Describe the morphology of the erythrocytes.
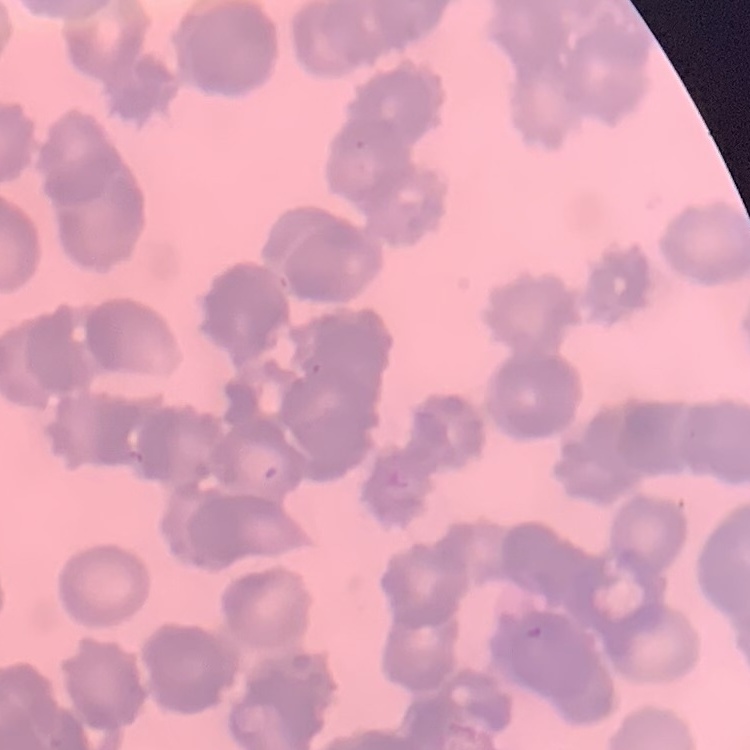

They show rouleaux formation.

preparation = thin blood smear
image type = one tile cut from a larger photomicrograph
stain = Field's or Giemsa